Classify this cell by malaria status.
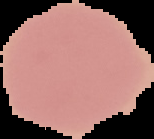

It is uninfected.

Summary:
  - Image type: segmented cell region with the area outside set to black
  - Image size: 154×139 pixels
  - Preparation: thin blood smear